Give the extent of all Trypanosoma brucei.
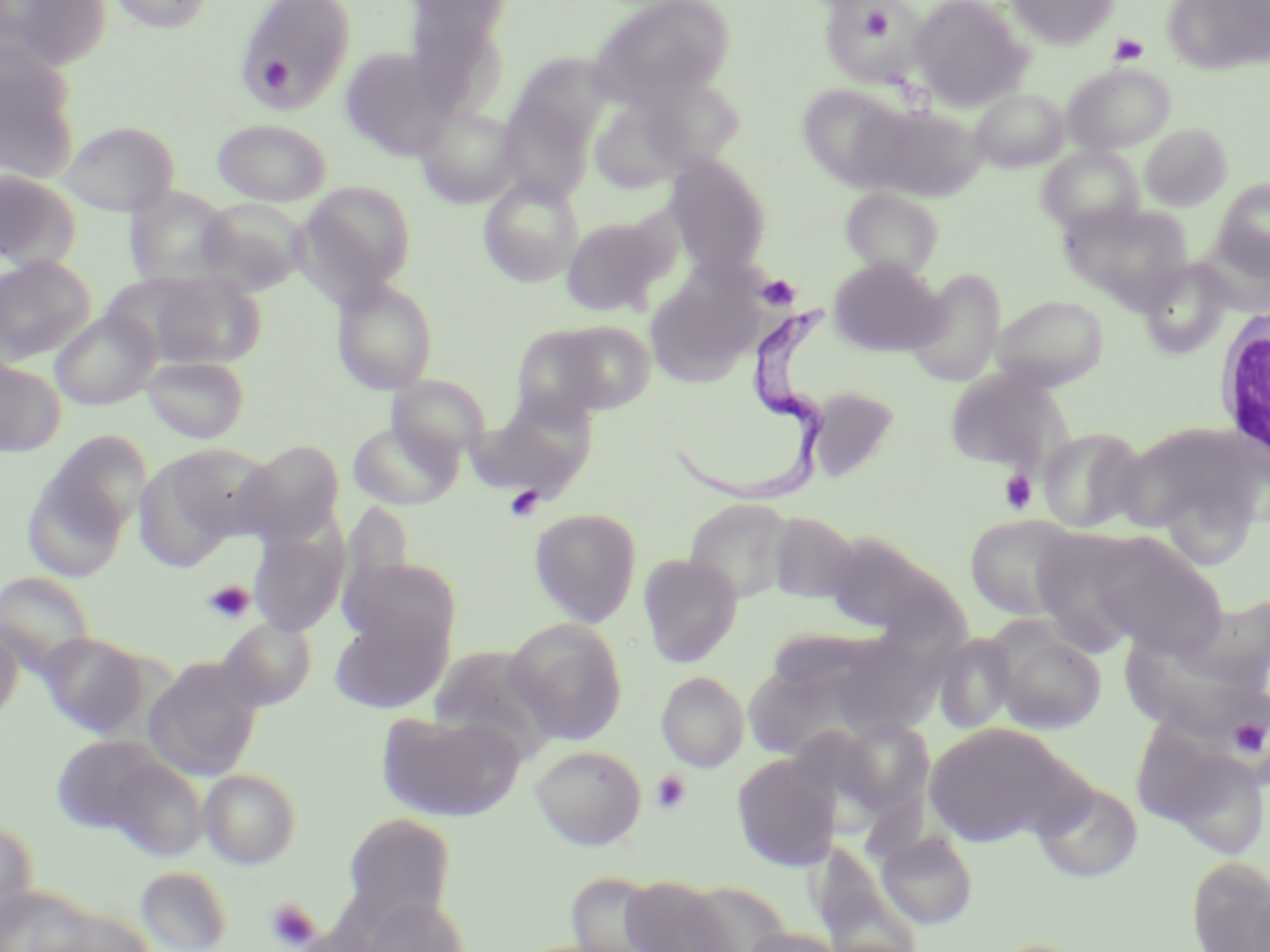
Approximate bounding boxes as named x1/y1/x2/y2 corners in pixels.
Trypanosoma brucei: (x1=667, y1=306, x2=833, y2=513).

Uninfected red blood cell locations: (x1=2, y1=0, x2=112, y2=71), (x1=108, y1=0, x2=215, y2=33), (x1=238, y1=0, x2=358, y2=110), (x1=407, y1=0, x2=513, y2=43), (x1=588, y1=0, x2=735, y2=109), (x1=910, y1=0, x2=1032, y2=111), (x1=1006, y1=0, x2=1117, y2=49), (x1=1162, y1=0, x2=1269, y2=74), (x1=827, y1=4, x2=920, y2=82), (x1=404, y1=7, x2=508, y2=115), (x1=0, y1=45, x2=82, y2=183), (x1=341, y1=47, x2=455, y2=160), (x1=512, y1=53, x2=615, y2=146), (x1=1063, y1=63, x2=1175, y2=155), (x1=638, y1=75, x2=746, y2=173), (x1=795, y1=83, x2=912, y2=189), (x1=971, y1=88, x2=1069, y2=172), (x1=496, y1=99, x2=593, y2=203), (x1=589, y1=99, x2=691, y2=194), (x1=856, y1=103, x2=986, y2=203), (x1=414, y1=105, x2=521, y2=209), (x1=212, y1=119, x2=332, y2=206), (x1=58, y1=120, x2=180, y2=216), (x1=1139, y1=122, x2=1233, y2=211), (x1=1037, y1=145, x2=1144, y2=236), (x1=664, y1=155, x2=772, y2=275), (x1=0, y1=171, x2=82, y2=271), (x1=478, y1=176, x2=583, y2=287), (x1=1214, y1=179, x2=1270, y2=276), (x1=296, y1=181, x2=416, y2=301), (x1=840, y1=187, x2=944, y2=279), (x1=125, y1=188, x2=235, y2=288), (x1=196, y1=198, x2=310, y2=296), (x1=1060, y1=202, x2=1193, y2=303), (x1=561, y1=217, x2=670, y2=316), (x1=1197, y1=236, x2=1270, y2=315), (x1=0, y1=256, x2=96, y2=364), (x1=828, y1=258, x2=945, y2=356), (x1=1138, y1=259, x2=1232, y2=359), (x1=907, y1=269, x2=1005, y2=387), (x1=145, y1=271, x2=266, y2=369), (x1=644, y1=271, x2=758, y2=388), (x1=101, y1=273, x2=222, y2=364), (x1=331, y1=278, x2=439, y2=395), (x1=991, y1=294, x2=1109, y2=391), (x1=50, y1=310, x2=158, y2=409), (x1=539, y1=321, x2=658, y2=415), (x1=141, y1=355, x2=250, y2=444), (x1=0, y1=360, x2=65, y2=456), (x1=943, y1=369, x2=1064, y2=473), (x1=387, y1=375, x2=490, y2=464), (x1=806, y1=386, x2=901, y2=483), (x1=473, y1=398, x2=597, y2=498), (x1=347, y1=420, x2=461, y2=511), (x1=1117, y1=423, x2=1266, y2=546), (x1=1038, y1=426, x2=1148, y2=533), (x1=236, y1=440, x2=346, y2=547), (x1=22, y1=442, x2=141, y2=580), (x1=159, y1=443, x2=279, y2=544), (x1=133, y1=449, x2=244, y2=573), (x1=683, y1=498, x2=796, y2=604), (x1=338, y1=499, x2=415, y2=623), (x1=529, y1=508, x2=641, y2=627), (x1=767, y1=512, x2=861, y2=604), (x1=964, y1=513, x2=1082, y2=621), (x1=248, y1=525, x2=347, y2=637), (x1=1027, y1=527, x2=1160, y2=653), (x1=1068, y1=530, x2=1229, y2=660), (x1=820, y1=531, x2=939, y2=635), (x1=638, y1=554, x2=742, y2=668), (x1=341, y1=555, x2=463, y2=663), (x1=0, y1=571, x2=96, y2=679), (x1=1186, y1=593, x2=1270, y2=695), (x1=329, y1=608, x2=452, y2=714), (x1=217, y1=618, x2=315, y2=710), (x1=505, y1=619, x2=628, y2=745), (x1=0, y1=620, x2=23, y2=725), (x1=988, y1=621, x2=1108, y2=734), (x1=38, y1=632, x2=149, y2=739), (x1=932, y1=632, x2=1018, y2=734), (x1=842, y1=640, x2=941, y2=742), (x1=428, y1=645, x2=561, y2=762), (x1=143, y1=656, x2=264, y2=781), (x1=741, y1=657, x2=872, y2=751), (x1=656, y1=671, x2=749, y2=772), (x1=376, y1=711, x2=524, y2=822), (x1=837, y1=718, x2=934, y2=815), (x1=924, y1=721, x2=1085, y2=847), (x1=1136, y1=729, x2=1270, y2=860), (x1=49, y1=735, x2=178, y2=840), (x1=530, y1=744, x2=647, y2=850), (x1=99, y1=754, x2=210, y2=864), (x1=732, y1=754, x2=840, y2=870), (x1=199, y1=768, x2=301, y2=869), (x1=1033, y1=778, x2=1144, y2=883), (x1=342, y1=812, x2=456, y2=928), (x1=0, y1=821, x2=38, y2=930), (x1=876, y1=829, x2=979, y2=929), (x1=1186, y1=855, x2=1270, y2=952), (x1=135, y1=866, x2=233, y2=952), (x1=564, y1=870, x2=673, y2=951), (x1=618, y1=877, x2=736, y2=952), (x1=680, y1=882, x2=792, y2=951), (x1=0, y1=884, x2=96, y2=951), (x1=360, y1=895, x2=471, y2=952), (x1=739, y1=925, x2=845, y2=952), (x1=988, y1=938, x2=1093, y2=952). White blood cell locations: (x1=1212, y1=301, x2=1270, y2=470). Platelet locations: (x1=858, y1=4, x2=896, y2=41), (x1=1109, y1=33, x2=1148, y2=64), (x1=258, y1=57, x2=294, y2=94), (x1=756, y1=274, x2=800, y2=311), (x1=999, y1=469, x2=1037, y2=515), (x1=505, y1=486, x2=544, y2=522), (x1=203, y1=580, x2=254, y2=625), (x1=1229, y1=716, x2=1266, y2=758), (x1=650, y1=770, x2=692, y2=816), (x1=266, y1=898, x2=321, y2=950). Slide-level diagnosis: Trypanosoma brucei. Thin blood smear. Light microscopy. May-Grünwald-Giemsa stain. Single field of view. Image is 1270×952 pixels. Captured at 1000x magnification.